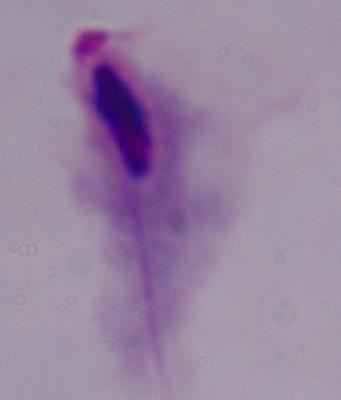

Micrograph. A trichomonad is seen. 1000x magnification.